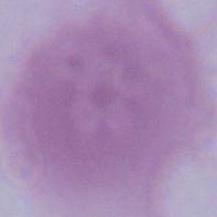

1000x magnification. Micrograph. An erythrocyte is seen.